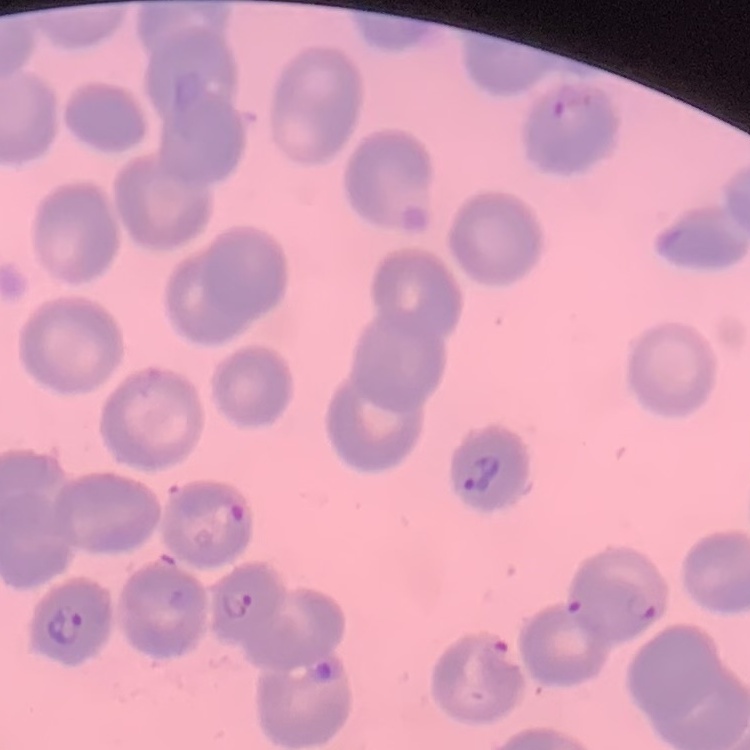

erythrocyte_morphology: no rouleaux formation
stain: Field's or Giemsa
image_type: square crop of a larger photomicrograph
preparation: thin blood film